Identify the parasite.
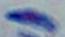
Toxoplasma gondii.

{
  "modality": "micrograph",
  "magnification": "1000x"
}